Assess the morphology of the red blood cells.
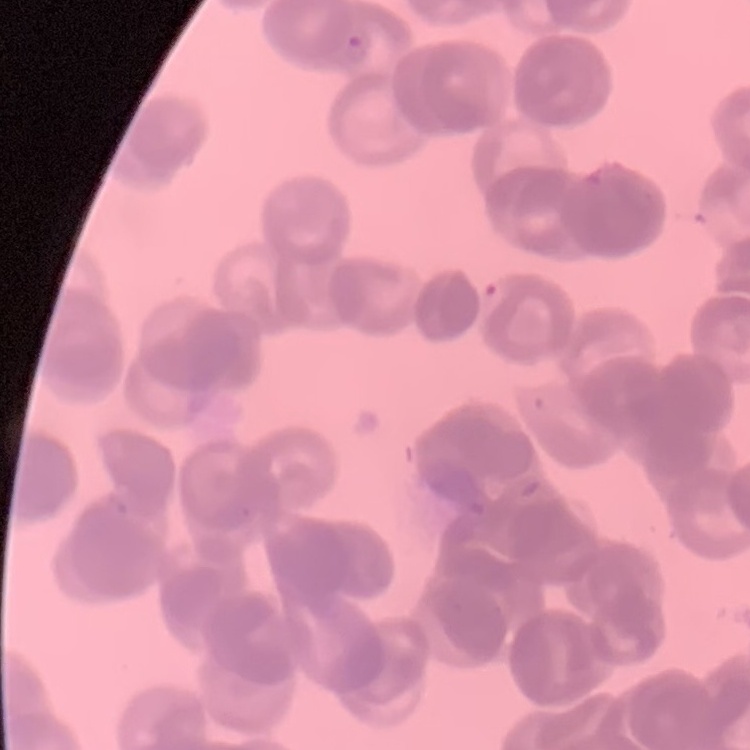
They show rouleaux formation.

image_type: square crop of a larger photomicrograph
stain: Field's or Giemsa
preparation: thin blood film